State which parasite is depicted.
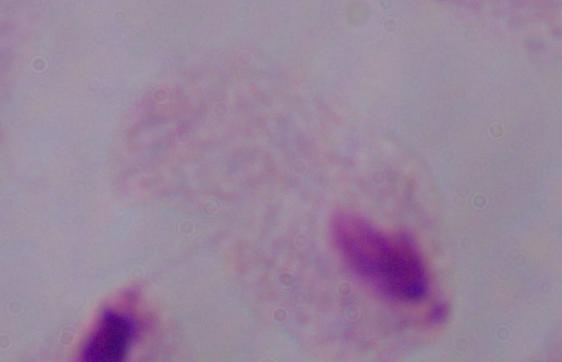
This is a trichomonad.

Summary:
  - Modality: micrograph
  - Magnification: 1000x